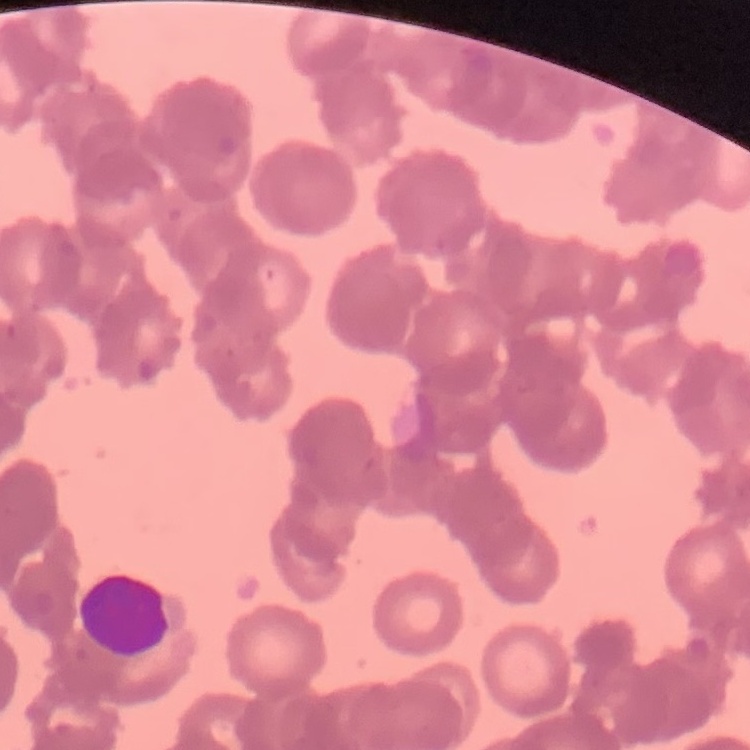

red blood cell morphology = rouleaux formation
preparation = thin blood film
image type = square crop of a larger photomicrograph
stain = Field's or Giemsa